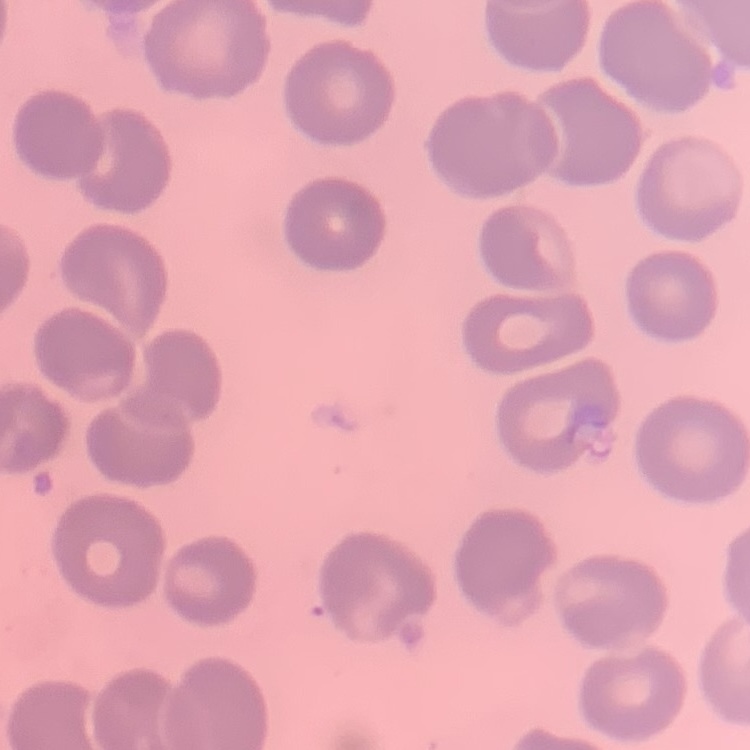
Summary:
  - Red blood cell morphology: no rouleaux formation
  - Image type: square crop of a larger photomicrograph
  - Preparation: thin blood film
  - Stain: Field's or Giemsa